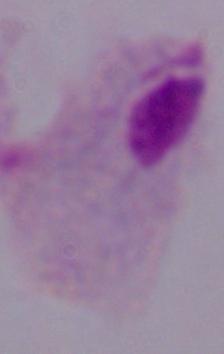
Summary:
  - Magnification: 1000x
  - Modality: photomicrograph
  - Identification: trichomonad